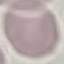
Malaria status: uninfected. Acquired by smartphone through the microscope eyepiece. Thin blood film. Giemsa stain. Automatically extracted cell patch, resized to 64 × 64 pixels.